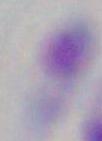
1000x magnification. Toxoplasma gondii is shown. Photomicrograph.